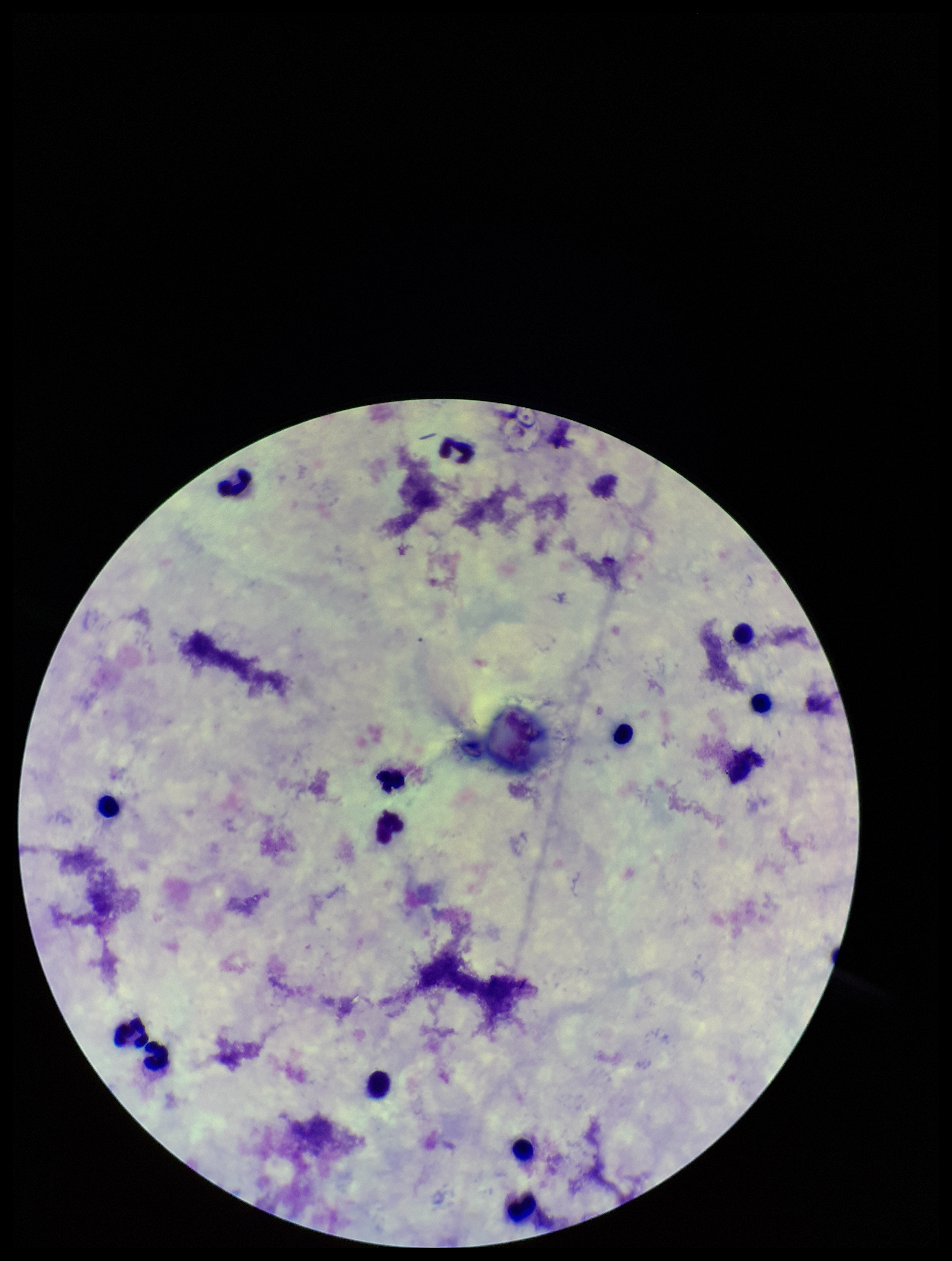

Summary:
  - Leukocyte count: 13
  - Plasmodium parasites: none detected
  - Stain: Giemsa
  - Patient malaria status: negative
  - Image size: 952×1261 pixels
  - Capture: smartphone photograph through the microscope eyepiece
  - Preparation: thick blood smear
  - Field of view: one from this slide
  - Parasite count: 0